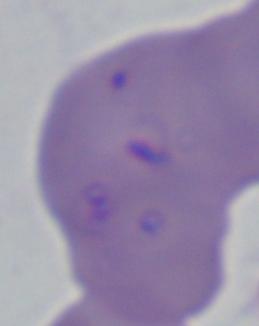
A Babesia parasite is seen. Photomicrograph. 1000x magnification.